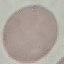
Summary:
  - Result: negative for malaria parasites
  - Preparation: thin blood film
  - Capture: smartphone camera at the microscope eyepiece
  - Stain: Giemsa
  - Image type: cell patch, automatically extracted from a larger field of view and resized to 64 × 64 pixels